Report the malaria status of this cell.
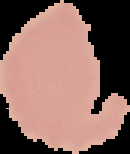
It is uninfected.

Summary:
  - Image type: segmented cell region with the area outside set to black
  - Image size: 130×154 pixels
  - Preparation: thin blood film